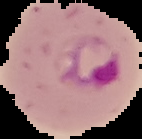

Segmented cell region on a black background. Result: malaria parasites identified. From a thin blood smear. Image is 142×139 pixels.